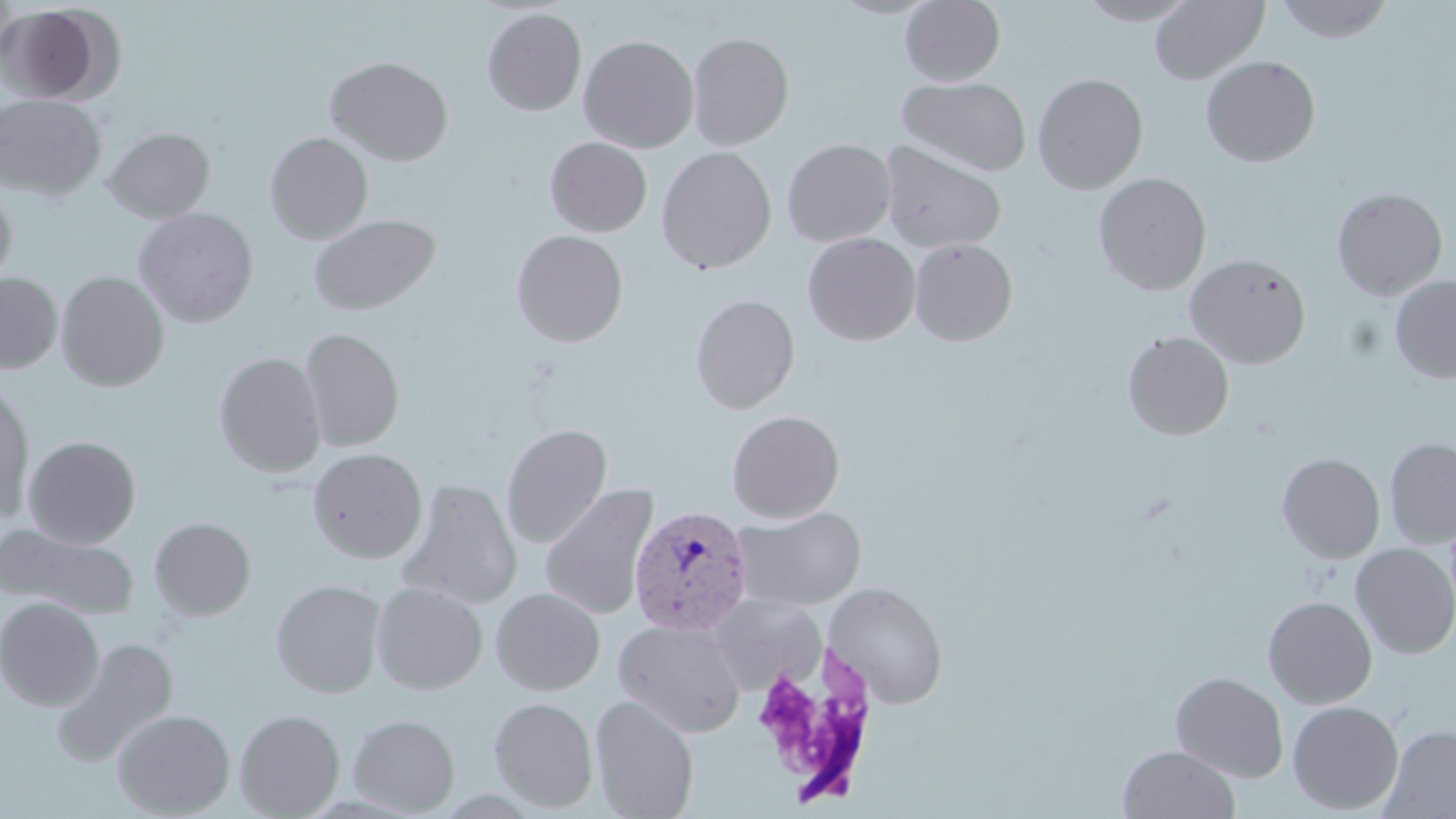

Approximate bounding boxes as (x1,y1)-(x2,y2) corner pairs in pixels. Plasmodium vivax-infected red blood cell locations: (628,505)-(754,635). Uninfected red blood cell locations: (900,0)-(1005,86), (1077,0)-(1196,26), (1150,0)-(1269,83), (1274,0)-(1394,43), (0,4)-(104,103), (482,8)-(586,116), (687,32)-(794,150), (578,34)-(699,153), (1200,55)-(1321,166), (326,56)-(453,165), (1032,72)-(1148,194), (897,76)-(1031,176), (0,95)-(106,200), (103,127)-(214,223), (117,127)-(239,301), (264,131)-(373,244), (544,136)-(652,237), (782,138)-(895,246), (877,141)-(1007,253), (657,146)-(776,274), (1094,172)-(1211,295), (0,185)-(17,288), (1331,187)-(1448,300), (133,207)-(259,329), (308,214)-(440,316), (511,229)-(628,347), (802,233)-(920,345), (909,238)-(1018,346), (1185,253)-(1311,369), (0,271)-(63,374), (56,271)-(169,391), (1390,274)-(1456,383), (690,293)-(800,414), (300,327)-(405,452), (1122,331)-(1234,440), (214,352)-(326,477), (0,379)-(35,526), (727,410)-(845,523), (500,422)-(612,548), (23,435)-(141,548), (1384,437)-(1456,549), (307,448)-(427,563), (1277,453)-(1385,563), (396,477)-(523,610), (540,482)-(659,621), (733,506)-(866,610), (149,516)-(256,620), (0,523)-(139,620), (1351,543)-(1456,659), (271,579)-(386,697), (370,582)-(488,694), (824,582)-(948,709), (491,587)-(605,695), (706,594)-(827,694), (1263,596)-(1377,708), (0,597)-(104,710), (613,619)-(747,738), (51,637)-(178,768), (1171,671)-(1288,781), (589,695)-(699,818), (489,696)-(598,812), (1287,700)-(1404,814), (111,708)-(235,817), (234,708)-(345,818), (348,713)-(460,816), (1380,725)-(1456,818), (1118,745)-(1241,819). Slide-level diagnosis: Plasmodium vivax. Optical microscopy. Image is 1456×819 pixels. Thin blood film. One field of a larger specimen. 1000x magnification. May-Grünwald-Giemsa-stained preparation.